Describe the morphology of the red blood cells.
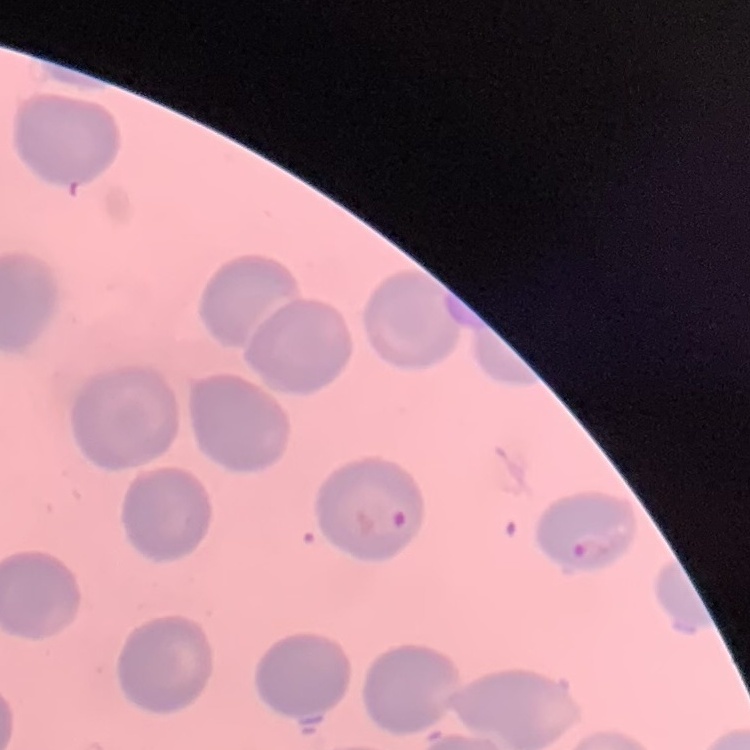

No rouleaux formation.

Thin blood smear. Square crop of a larger photomicrograph. Stained with either Field's or Giemsa.